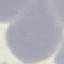
result = no malaria parasites detected
stain = Giemsa
capture = smartphone through the microscope eyepiece
preparation = thin blood film
image type = cell patch, automatically extracted from a larger field of view and resized to 64 × 64 pixels